Assess this cell for malaria.
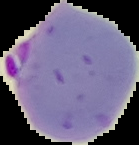

Parasitized.

image size = 139×145 pixels
image type = segmented cell region with the area outside set to black
preparation = thin blood film